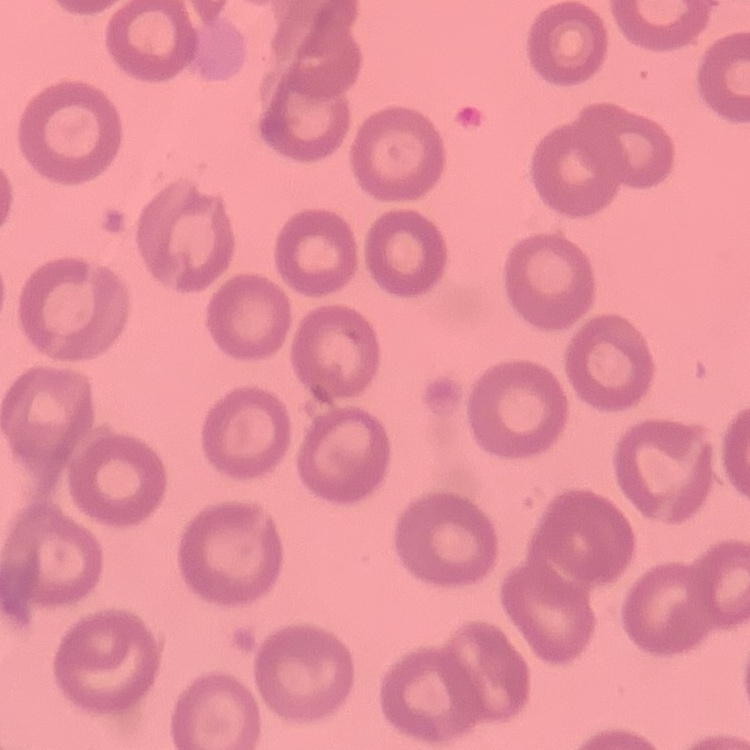 The red blood cells show no rouleaux formation. Square crop of a larger photomicrograph. Field's or Giemsa stain. Thin peripheral smear.